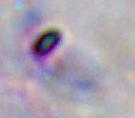

Summary:
  - Identification: Toxoplasma gondii
  - Magnification: 1000x
  - Modality: photomicrograph